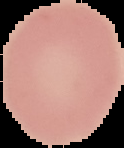
Summary:
  - Image type: cell region segmented out of the field of view; surrounding area masked to black
  - Image size: 124×148 pixels
  - Preparation: thin blood film
  - Malaria status: uninfected